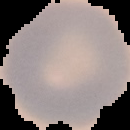
Summary:
  - Preparation: thin blood film
  - Image size: 130×130 pixels
  - Image type: segmented cell region on a black background
  - Result: no Plasmodium parasites seen